Give the extent of all Plasmodium falciparum-infected red blood cells.
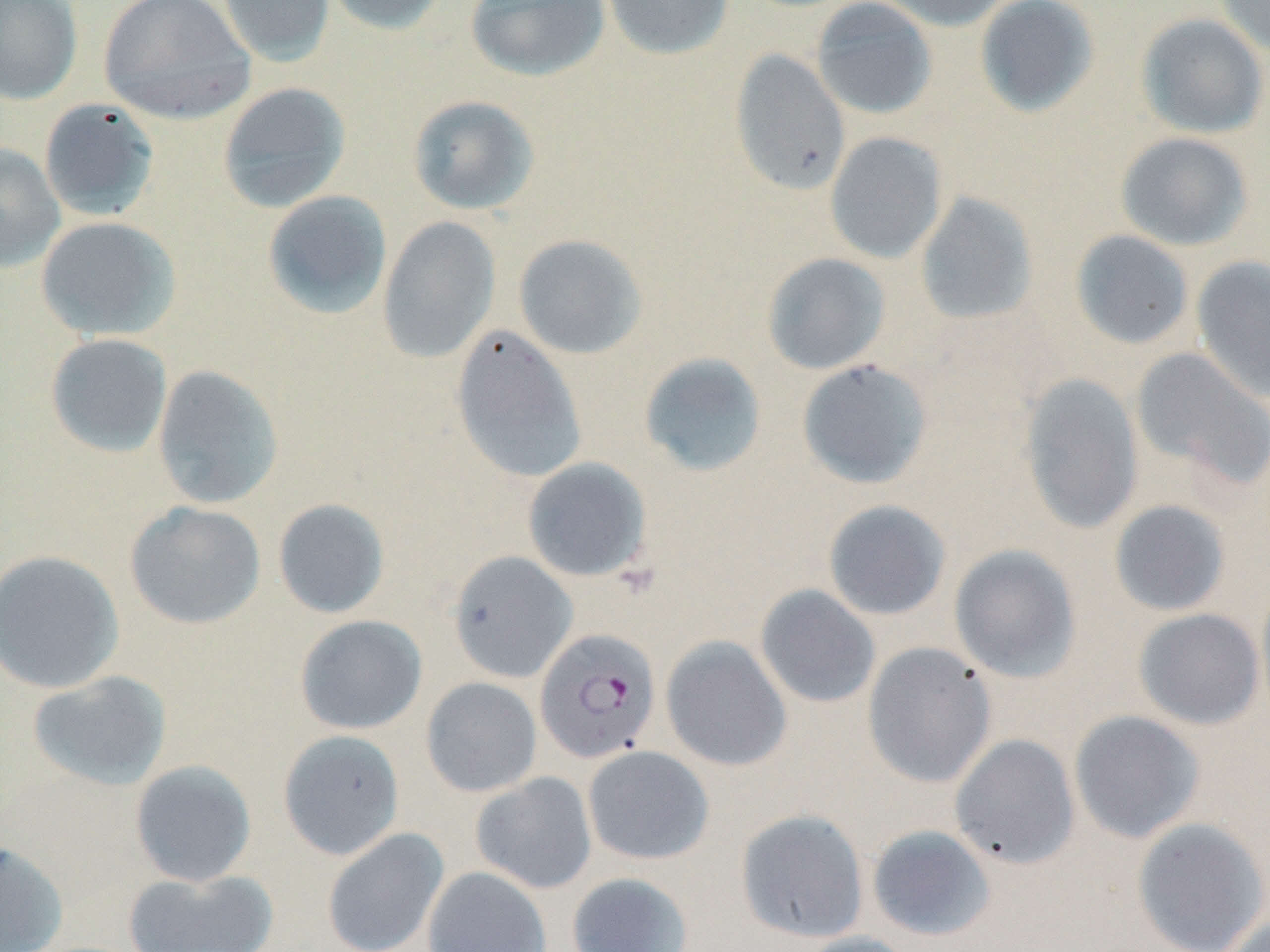

Approximate bounding boxes as (x1,y1)-(x2,y2) corner pairs in pixels.
Plasmodium falciparum-infected red blood cells: (535,628)-(661,764).

{
  "slide_level_diagnosis": "Plasmodium falciparum",
  "magnification": "1000x",
  "preparation": "thin blood smear",
  "stain": "May-Grünwald-Giemsa",
  "image_size": "1270×952 pixels",
  "field_of_view": "one of a larger specimen",
  "modality": "light microscopy",
  "uninfected_red_blood_cell_locations": "approximate bounding boxes as (x1,y1)-(x2,y2) corner pairs in pixels: (0,0)-(83,105), (97,0)-(256,125), (217,0)-(335,67), (321,0)-(451,35), (465,0)-(610,82), (601,0)-(734,60), (810,0)-(938,120), (876,0)-(1016,31), (974,0)-(1100,118), (1214,0)-(1270,57), (1136,13)-(1269,139), (729,49)-(851,196), (217,82)-(352,213), (407,95)-(541,216), (38,99)-(160,222), (825,131)-(947,264), (1115,132)-(1254,251), (0,143)-(66,274), (262,190)-(393,320), (914,192)-(1039,326), (377,215)-(501,364), (35,216)-(181,341), (1070,229)-(1195,350), (513,234)-(648,360), (761,253)-(891,375), (1191,256)-(1270,403), (450,325)-(588,485), (44,333)-(173,458), (1131,347)-(1270,492), (638,353)-(768,478), (796,359)-(934,489), (151,364)-(285,510), (1018,372)-(1144,534), (522,457)-(653,583), (272,498)-(390,619), (822,499)-(952,621), (1108,499)-(1232,617), (124,501)-(267,630), (949,544)-(1082,683), (0,550)-(125,695), (448,551)-(578,683), (1255,580)-(1270,723), (755,584)-(881,709), (1133,608)-(1265,730), (294,615)-(428,735), (661,635)-(792,772), (862,642)-(997,788), (27,670)-(172,791), (420,677)-(542,797), (1069,710)-(1205,844), (277,730)-(405,860), (949,733)-(1081,870), (582,745)-(715,865), (129,759)-(258,887), (471,772)-(597,894), (735,808)-(870,943), (1131,817)-(1269,952), (866,824)-(997,942), (322,827)-(449,952), (0,840)-(68,952), (423,865)-(552,952), (123,867)-(278,952), (566,872)-(694,952), (1218,913)-(1270,952), (792,932)-(920,952)"
}